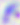 400x magnification. Toxoplasma gondii is shown. Photomicrograph.